Give the position of every malaria parasite and every leukocyte.
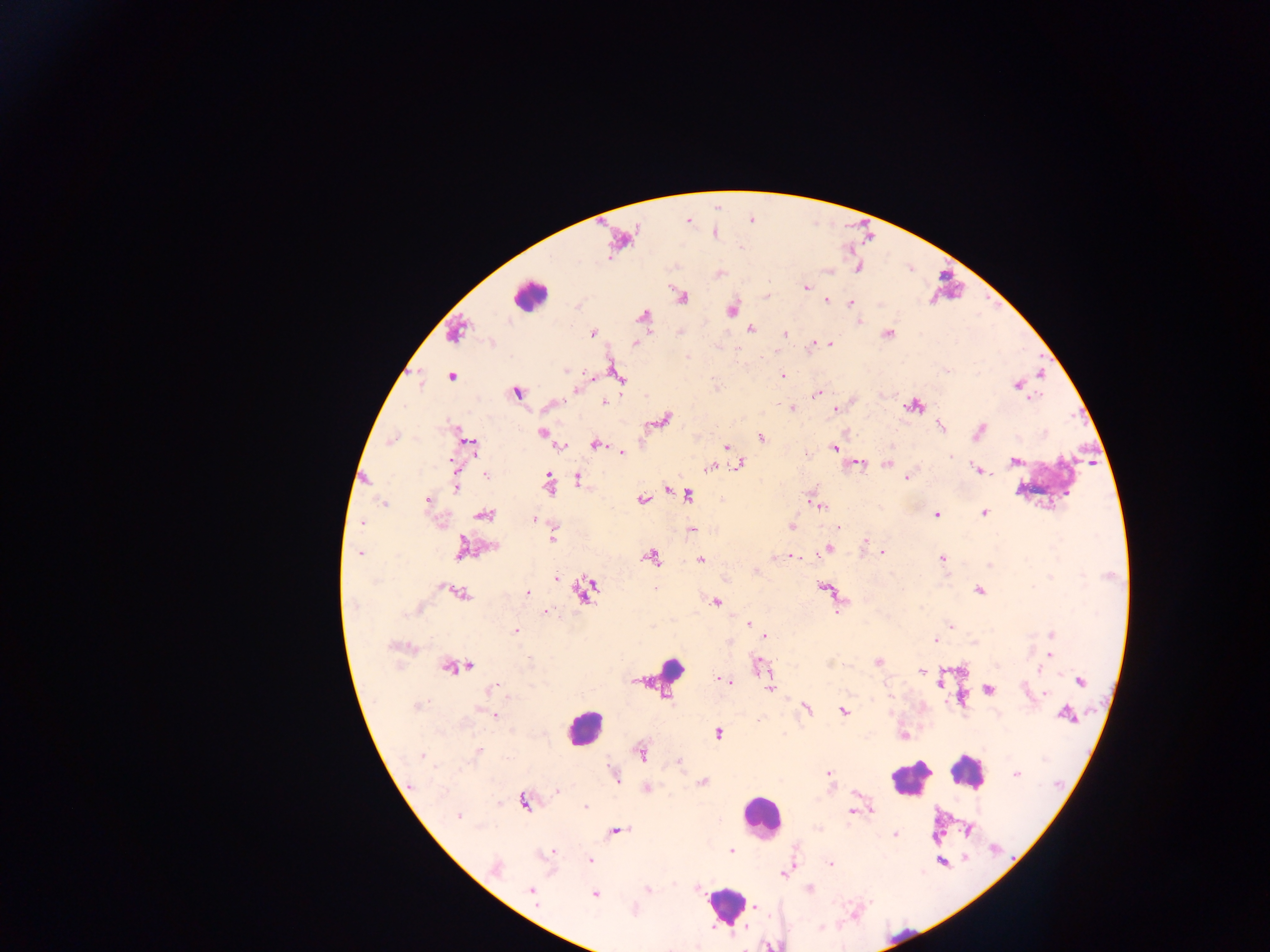

Approximate centers as (x, y) in pixels.
Malaria parasites: (806, 287), (827, 300), (851, 303), (750, 329), (593, 333), (784, 333), (814, 343), (829, 343), (635, 344), (565, 371), (782, 375), (451, 376), (1018, 384), (576, 389), (516, 392), (817, 394), (1032, 397), (605, 403), (792, 408), (836, 408), (664, 419), (940, 426), (980, 431), (542, 432), (761, 438), (392, 440), (471, 444), (595, 444), (726, 446), (562, 447), (835, 447), (622, 453), (950, 457), (1014, 461), (451, 462), (858, 463), (887, 463), (739, 465), (710, 467), (978, 470), (486, 475), (549, 478), (577, 478), (907, 478), (457, 488), (666, 489), (687, 496), (641, 499), (428, 500), (384, 505), (821, 506), (985, 513), (485, 514), (937, 515), (534, 519), (362, 523), (792, 527), (838, 528), (553, 539), (864, 540), (462, 547), (493, 547), (829, 549), (883, 553), (359, 554), (793, 557), (651, 558), (701, 559), (942, 559), (756, 571), (556, 578), (654, 588), (980, 590), (461, 593), (526, 594), (716, 602), (355, 606), (546, 611), (748, 624), (951, 627), (516, 631), (1051, 634), (765, 636), (935, 640), (1050, 653), (529, 660), (878, 661), (759, 664), (467, 667), (1039, 668), (922, 671), (725, 681), (1081, 681), (940, 683), (770, 688), (491, 689), (988, 690), (1045, 694), (418, 705), (806, 709), (844, 711), (493, 715), (1067, 715), (758, 721), (718, 733), (477, 752), (641, 753), (422, 755), (678, 761), (828, 772), (1015, 774), (615, 775), (703, 782), (646, 788), (557, 791), (499, 802), (525, 803), (585, 807), (871, 811), (851, 812), (458, 816), (617, 831), (895, 834), (731, 849), (552, 851), (590, 860), (830, 864), (495, 867), (784, 873), (647, 889), (531, 890), (809, 890), (594, 894), (821, 927).
Leukocytes (some below the resolvable threshold): (623, 237), (529, 296), (1051, 477), (668, 665), (583, 727), (966, 772), (910, 779), (761, 815), (725, 905).

Summary:
  - Country: Ghana
  - Capture: mobile-phone photograph through a microscope
  - Field of view: single
  - Image size: 1270×952 pixels
  - Preparation: thick blood smear